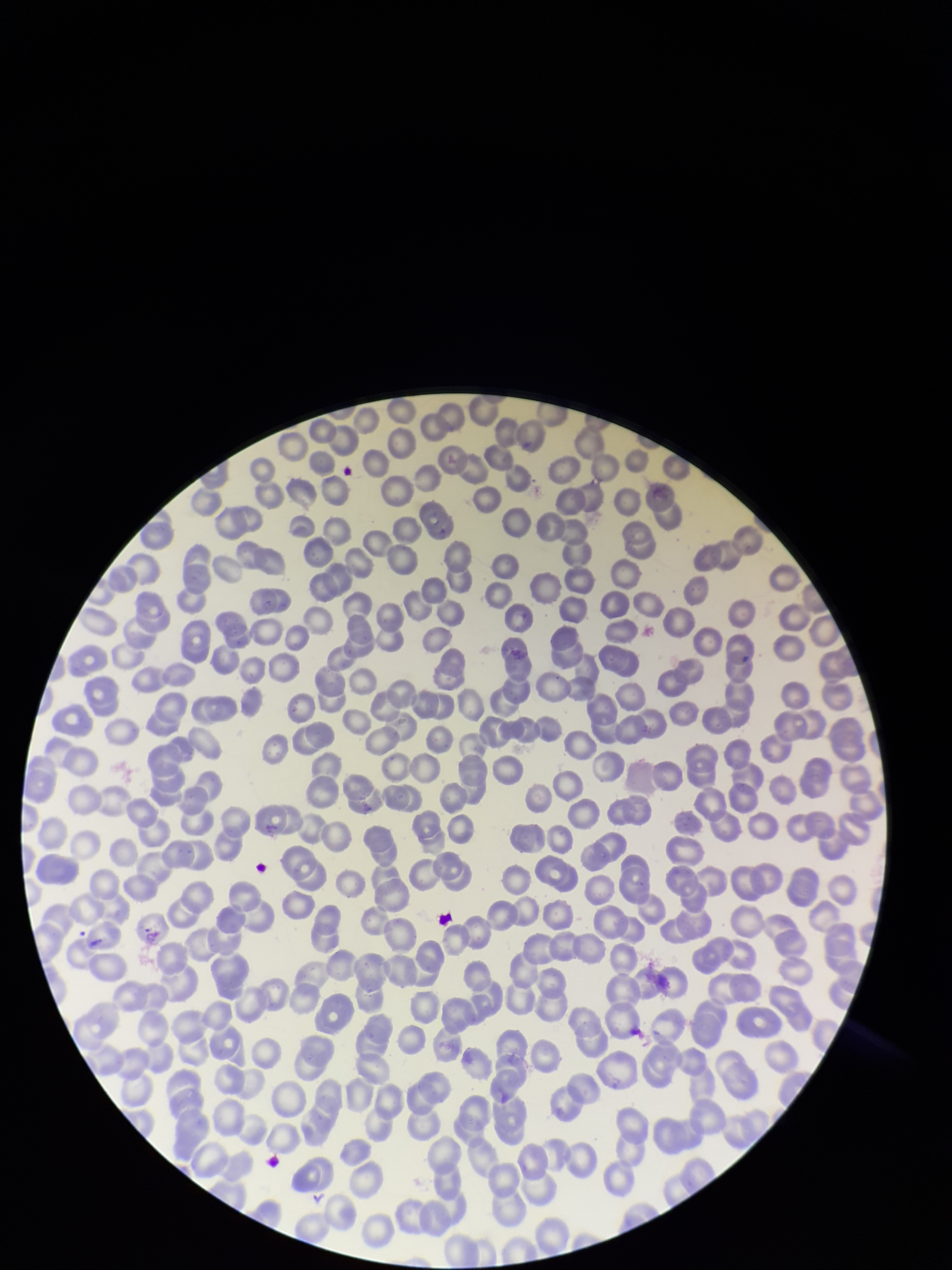
Summary:
  - Red blood cell count: 260
  - Parasitized red blood cell count: 0
  - Parasitized red blood cells: none detected
  - Image size: 952×1270 pixels
  - Capture: smartphone photograph through the microscope eyepiece
  - Patient malaria status: negative
  - Stain: Giemsa
  - Field of view: single
  - Preparation: thin blood smear